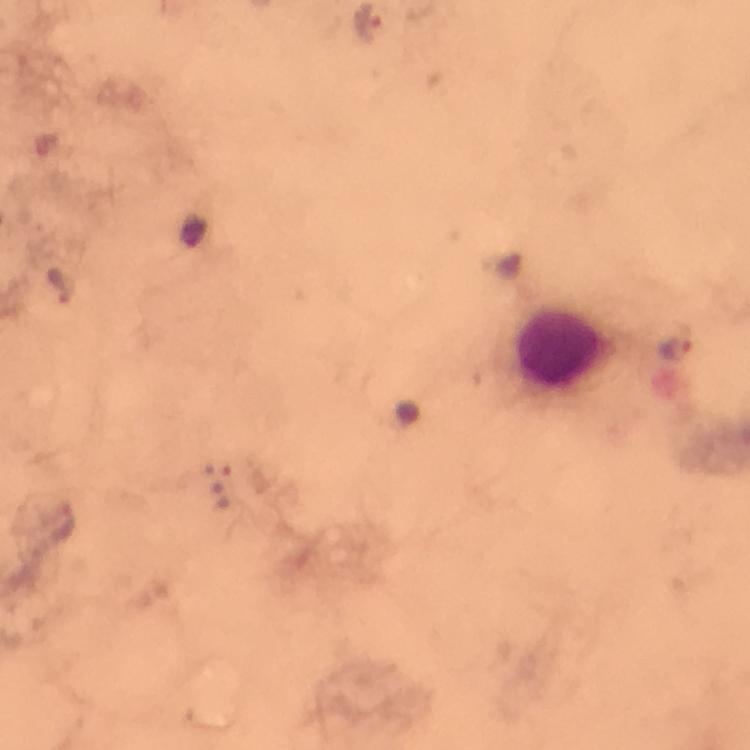
image size = 750×750 pixels
immersion oil = applied
magnification = 100x
preparation = thick blood smear
malaria parasite locations = approximate object centers, in pixels from the top-left corner: (x=55, y=282), (x=677, y=349)
leukocyte locations = approximate object centers, in pixels from the top-left corner: (x=565, y=358)
cropped from = one field of view
capture = smartphone camera through the microscope
context = from a malaria diagnostic workup
stain = Giemsa